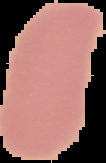
{
  "image_type": "cell region segmented out of the field of view; surrounding area masked to black",
  "preparation": "thin blood film",
  "image_size": "106×163 pixels",
  "result": "negative for Plasmodium parasites"
}